Classify this cell by malaria status.
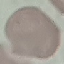

It is uninfected.

Summary:
  - Image type: cell patch, automatically extracted from a larger field of view and resized to 64 × 64 pixels
  - Stain: Giemsa
  - Preparation: thin smear
  - Capture: smartphone camera at the microscope eyepiece